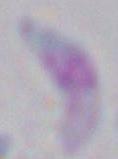

1000x magnification. Toxoplasma gondii is shown. Photomicrograph.